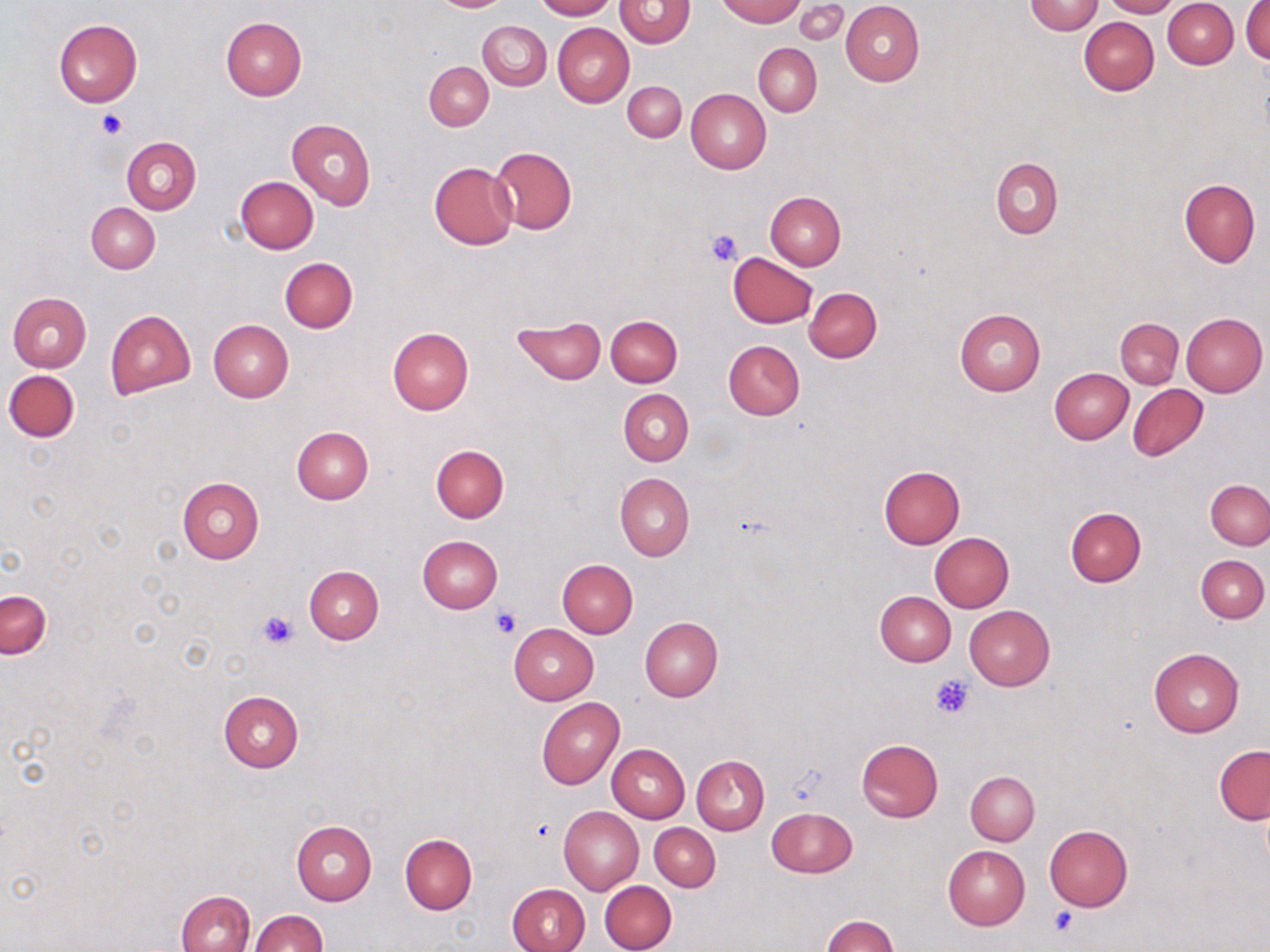

Approximate bounding boxes as named x1/y1/x2/y2 corners in pixels. Uninfected red blood cell locations: (x1=427, y1=0, x2=513, y2=12), (x1=533, y1=0, x2=615, y2=20), (x1=718, y1=0, x2=803, y2=25), (x1=796, y1=0, x2=846, y2=42), (x1=1101, y1=0, x2=1178, y2=18), (x1=615, y1=1, x2=695, y2=48), (x1=841, y1=1, x2=925, y2=86), (x1=1024, y1=1, x2=1103, y2=35), (x1=1163, y1=1, x2=1238, y2=69), (x1=1242, y1=2, x2=1270, y2=64), (x1=1079, y1=16, x2=1159, y2=95), (x1=221, y1=17, x2=307, y2=100), (x1=54, y1=18, x2=143, y2=106), (x1=478, y1=20, x2=551, y2=90), (x1=552, y1=23, x2=633, y2=109), (x1=754, y1=43, x2=822, y2=116), (x1=424, y1=61, x2=493, y2=130), (x1=623, y1=81, x2=685, y2=142), (x1=686, y1=88, x2=770, y2=174), (x1=286, y1=118, x2=375, y2=211), (x1=123, y1=137, x2=201, y2=215), (x1=490, y1=146, x2=577, y2=234), (x1=991, y1=157, x2=1063, y2=238), (x1=429, y1=161, x2=518, y2=249), (x1=235, y1=176, x2=319, y2=254), (x1=1179, y1=178, x2=1260, y2=267), (x1=766, y1=192, x2=845, y2=270), (x1=86, y1=202, x2=160, y2=273), (x1=728, y1=252, x2=817, y2=328), (x1=279, y1=258, x2=357, y2=333), (x1=804, y1=287, x2=882, y2=363), (x1=8, y1=292, x2=91, y2=372), (x1=954, y1=308, x2=1045, y2=395), (x1=105, y1=310, x2=195, y2=399), (x1=1181, y1=312, x2=1268, y2=396), (x1=606, y1=315, x2=682, y2=387), (x1=511, y1=317, x2=607, y2=384), (x1=1115, y1=318, x2=1183, y2=388), (x1=207, y1=320, x2=293, y2=403), (x1=387, y1=328, x2=474, y2=414), (x1=723, y1=339, x2=804, y2=419), (x1=1048, y1=368, x2=1133, y2=444), (x1=4, y1=369, x2=80, y2=441), (x1=1128, y1=385, x2=1209, y2=462), (x1=619, y1=389, x2=693, y2=466), (x1=291, y1=427, x2=373, y2=504), (x1=431, y1=444, x2=509, y2=523), (x1=878, y1=465, x2=965, y2=548), (x1=615, y1=473, x2=695, y2=561), (x1=177, y1=476, x2=264, y2=564), (x1=1205, y1=478, x2=1270, y2=550), (x1=1065, y1=506, x2=1147, y2=586), (x1=930, y1=532, x2=1014, y2=611), (x1=417, y1=535, x2=503, y2=612), (x1=1196, y1=554, x2=1268, y2=622), (x1=557, y1=559, x2=638, y2=637), (x1=304, y1=566, x2=383, y2=645), (x1=1, y1=591, x2=50, y2=658), (x1=875, y1=591, x2=956, y2=666), (x1=964, y1=605, x2=1056, y2=690), (x1=639, y1=618, x2=723, y2=702), (x1=509, y1=624, x2=598, y2=704), (x1=1149, y1=648, x2=1244, y2=737), (x1=218, y1=691, x2=303, y2=773), (x1=536, y1=697, x2=624, y2=790), (x1=856, y1=738, x2=943, y2=822), (x1=607, y1=744, x2=689, y2=823), (x1=1214, y1=745, x2=1270, y2=825), (x1=692, y1=755, x2=769, y2=834), (x1=966, y1=770, x2=1040, y2=845), (x1=766, y1=806, x2=857, y2=878), (x1=558, y1=807, x2=643, y2=894), (x1=291, y1=820, x2=377, y2=905), (x1=650, y1=822, x2=721, y2=890), (x1=1044, y1=824, x2=1133, y2=911), (x1=400, y1=834, x2=477, y2=915), (x1=943, y1=844, x2=1030, y2=928), (x1=600, y1=880, x2=677, y2=952), (x1=507, y1=883, x2=589, y2=952), (x1=176, y1=890, x2=254, y2=952), (x1=250, y1=910, x2=325, y2=951), (x1=822, y1=915, x2=897, y2=952). Platelet locations: (x1=97, y1=107, x2=127, y2=138), (x1=706, y1=227, x2=744, y2=265), (x1=490, y1=603, x2=522, y2=638), (x1=256, y1=609, x2=299, y2=649), (x1=931, y1=674, x2=974, y2=718), (x1=528, y1=815, x2=558, y2=842), (x1=1049, y1=904, x2=1081, y2=938). Slide-level diagnosis: negative for blood parasites. Image is 1270×952 pixels. One field of a larger specimen. Optical microscopy. Thin blood film. 1000x magnification. May-Grünwald-Giemsa-stained preparation.